Locate and identify every blood parasite.
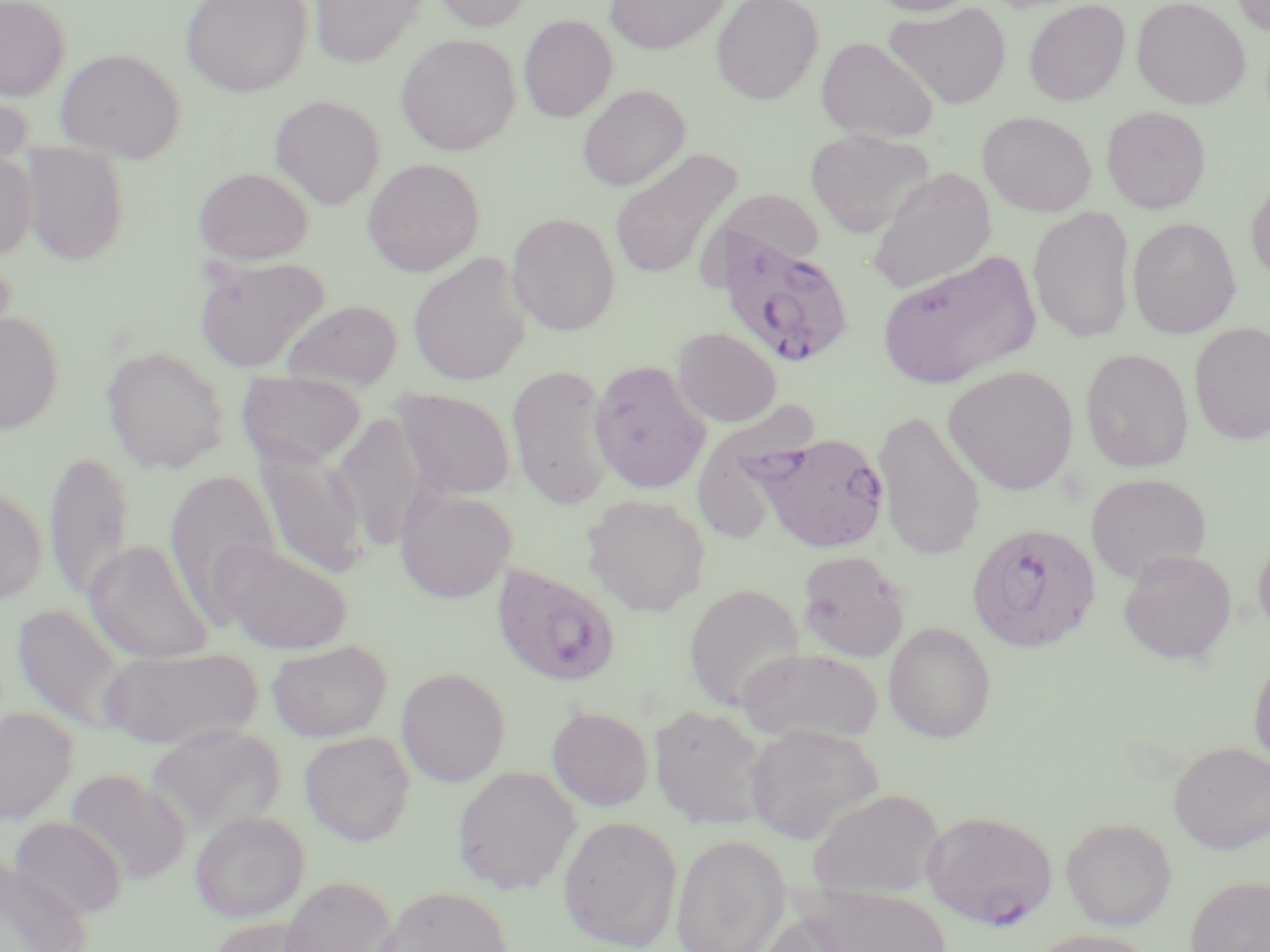

Approximate bounding boxes as named x1/y1/x2/y2 corners in pixels.
Plasmodium falciparum-infected red blood cells: (x1=715, y1=227, x2=856, y2=371), (x1=749, y1=430, x2=891, y2=553), (x1=966, y1=522, x2=1101, y2=652), (x1=490, y1=562, x2=622, y2=688), (x1=922, y1=811, x2=1056, y2=929).
No Plasmodium ovale, Plasmodium malariae, Plasmodium vivax, Babesia divergens, or Trypanosoma brucei observed.

slide-level diagnosis = Plasmodium falciparum
preparation = thin blood smear
stain = May-Grünwald-Giemsa
magnification = 1000x
uninfected red blood cell locations = approximate bounding boxes as named x1/y1/x2/y2 corners in pixels: (x1=0, y1=0, x2=70, y2=101), (x1=181, y1=0, x2=313, y2=98), (x1=430, y1=0, x2=535, y2=32), (x1=604, y1=0, x2=730, y2=54), (x1=711, y1=0, x2=823, y2=105), (x1=864, y1=0, x2=981, y2=16), (x1=1024, y1=0, x2=1131, y2=106), (x1=1131, y1=0, x2=1251, y2=109), (x1=1231, y1=0, x2=1270, y2=36), (x1=308, y1=1, x2=428, y2=68), (x1=884, y1=2, x2=1012, y2=109), (x1=518, y1=14, x2=617, y2=123), (x1=396, y1=33, x2=520, y2=155), (x1=816, y1=37, x2=938, y2=143), (x1=55, y1=47, x2=186, y2=162), (x1=576, y1=84, x2=690, y2=191), (x1=0, y1=87, x2=34, y2=179), (x1=269, y1=95, x2=385, y2=210), (x1=1101, y1=105, x2=1211, y2=213), (x1=977, y1=111, x2=1096, y2=216), (x1=805, y1=130, x2=934, y2=239), (x1=20, y1=143, x2=130, y2=265), (x1=608, y1=148, x2=743, y2=283), (x1=0, y1=151, x2=38, y2=260), (x1=362, y1=158, x2=485, y2=277), (x1=193, y1=166, x2=314, y2=264), (x1=867, y1=168, x2=996, y2=296), (x1=1246, y1=173, x2=1270, y2=287), (x1=712, y1=189, x2=826, y2=271), (x1=1028, y1=206, x2=1135, y2=343), (x1=507, y1=212, x2=621, y2=336), (x1=1127, y1=217, x2=1241, y2=338), (x1=875, y1=250, x2=1042, y2=390), (x1=408, y1=252, x2=531, y2=387), (x1=192, y1=254, x2=331, y2=373), (x1=282, y1=299, x2=403, y2=390), (x1=0, y1=312, x2=65, y2=434), (x1=1189, y1=322, x2=1270, y2=445), (x1=673, y1=327, x2=781, y2=427), (x1=101, y1=344, x2=229, y2=475), (x1=1080, y1=348, x2=1194, y2=473), (x1=589, y1=360, x2=711, y2=494), (x1=507, y1=364, x2=616, y2=510), (x1=943, y1=365, x2=1079, y2=495), (x1=236, y1=372, x2=368, y2=469), (x1=392, y1=388, x2=516, y2=501), (x1=695, y1=403, x2=821, y2=538), (x1=873, y1=409, x2=986, y2=561), (x1=332, y1=412, x2=430, y2=552), (x1=254, y1=444, x2=369, y2=579), (x1=44, y1=449, x2=134, y2=603), (x1=164, y1=468, x2=281, y2=620), (x1=1085, y1=472, x2=1212, y2=584), (x1=394, y1=485, x2=517, y2=603), (x1=0, y1=486, x2=47, y2=604), (x1=582, y1=494, x2=711, y2=616), (x1=1252, y1=534, x2=1270, y2=644), (x1=84, y1=539, x2=214, y2=664), (x1=218, y1=542, x2=353, y2=654), (x1=1118, y1=549, x2=1237, y2=664), (x1=796, y1=550, x2=911, y2=663), (x1=684, y1=583, x2=805, y2=710), (x1=11, y1=603, x2=132, y2=734), (x1=882, y1=621, x2=996, y2=742), (x1=268, y1=639, x2=392, y2=742), (x1=97, y1=645, x2=263, y2=748), (x1=736, y1=646, x2=885, y2=745), (x1=1249, y1=650, x2=1270, y2=770), (x1=396, y1=667, x2=511, y2=787), (x1=649, y1=703, x2=773, y2=830), (x1=0, y1=707, x2=78, y2=824), (x1=546, y1=707, x2=654, y2=811), (x1=743, y1=723, x2=884, y2=844), (x1=145, y1=724, x2=286, y2=836), (x1=299, y1=730, x2=416, y2=846), (x1=1169, y1=741, x2=1270, y2=853), (x1=452, y1=765, x2=582, y2=894), (x1=65, y1=769, x2=191, y2=885), (x1=808, y1=788, x2=944, y2=899), (x1=189, y1=810, x2=309, y2=922), (x1=10, y1=815, x2=127, y2=920), (x1=558, y1=815, x2=683, y2=951), (x1=1061, y1=816, x2=1177, y2=930), (x1=671, y1=834, x2=790, y2=952), (x1=0, y1=854, x2=93, y2=952), (x1=1185, y1=875, x2=1270, y2=952), (x1=276, y1=876, x2=399, y2=952), (x1=795, y1=883, x2=952, y2=952), (x1=377, y1=885, x2=514, y2=952), (x1=754, y1=913, x2=862, y2=952), (x1=205, y1=916, x2=323, y2=952), (x1=1027, y1=929, x2=1157, y2=952)
image size = 1270×952 pixels
field of view = single
modality = optical microscopy